Report the malaria status.
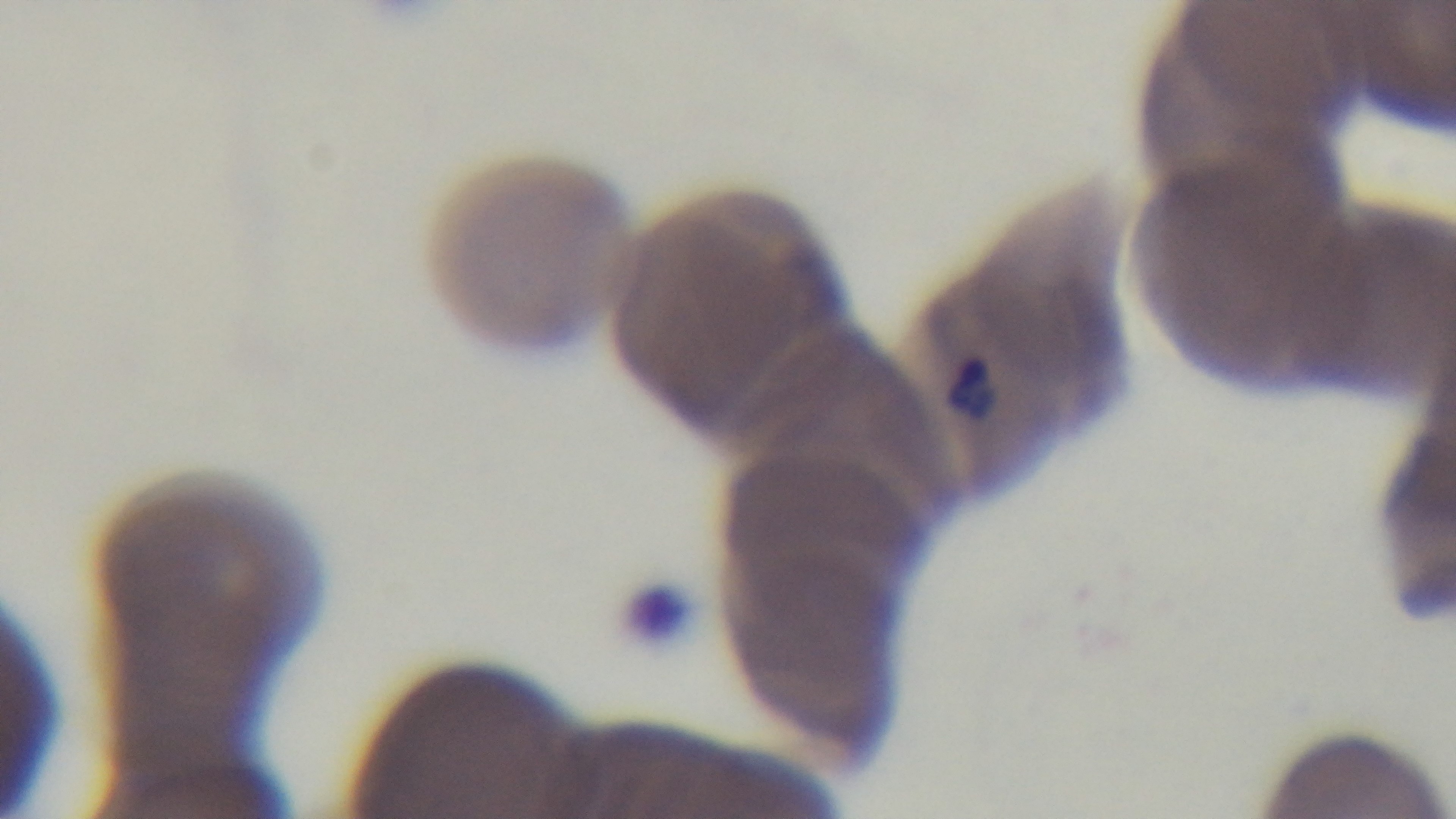
Infected.

Summary:
  - Objective: 100x oil immersion
  - Field of view: single
  - Stain: Giemsa
  - Preparation: thin blood film
  - Modality: light microscopy
  - Capture: mounted 4K digital camera